Assess this cell for malaria.
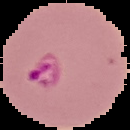
It is parasitized.

Cell region segmented out of the field of view; the surrounding area is masked to black. Image is 130×130 pixels. From a thin blood film.